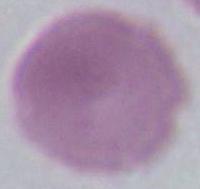

magnification = 1000x
modality = micrograph
identification = erythrocyte